Classify this cell by malaria status.
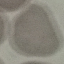
It is uninfected.

image type = automatically extracted cell patch, resized to 64 × 64 pixels
capture = smartphone camera at the microscope eyepiece
stain = Giemsa
preparation = thin blood smear